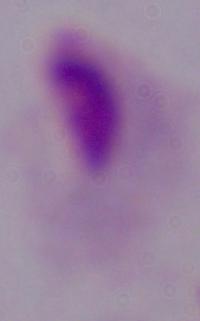
Summary:
  - Magnification: 1000x
  - Identification: trichomonad
  - Modality: photomicrograph